Assess this cell for malaria.
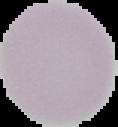
It is uninfected.

preparation = thin blood film
image size = 118×127 pixels
image type = cell region segmented out of the field of view; surrounding area masked to black